Assess this cell for malaria.
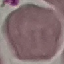
It is uninfected.

image type = cell patch, automatically extracted from a larger field of view and resized to 64 × 64 pixels
preparation = thin smear
stain = Giemsa
capture = smartphone through the microscope eyepiece